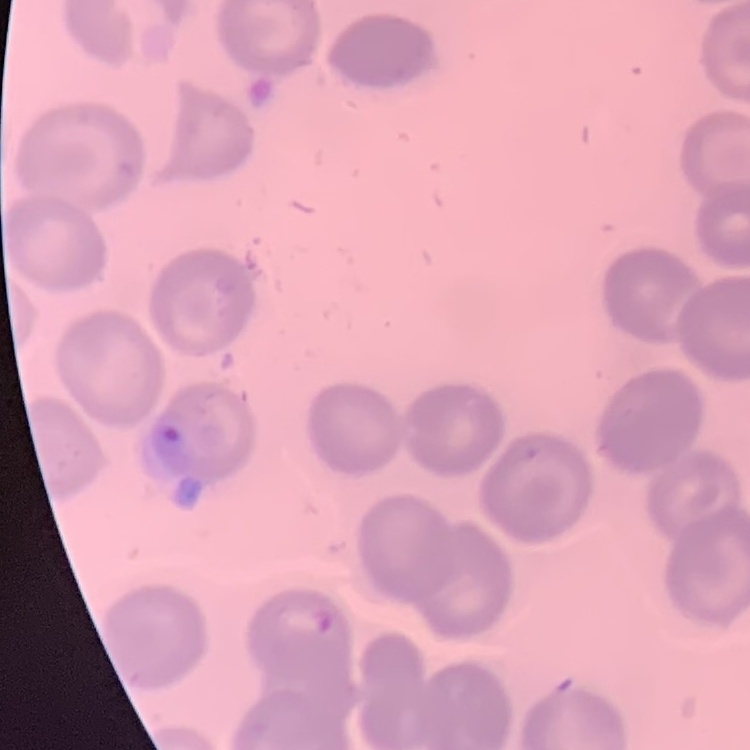

Summary:
  - Erythrocyte morphology: no rouleaux formation
  - Preparation: thin blood film
  - Image type: one tile cut from a larger photomicrograph
  - Stain: Field's or Giemsa